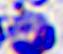

Summary:
  - Identification: leukocyte
  - Modality: micrograph
  - Magnification: 400x